Give a bounding box for every gametocyte.
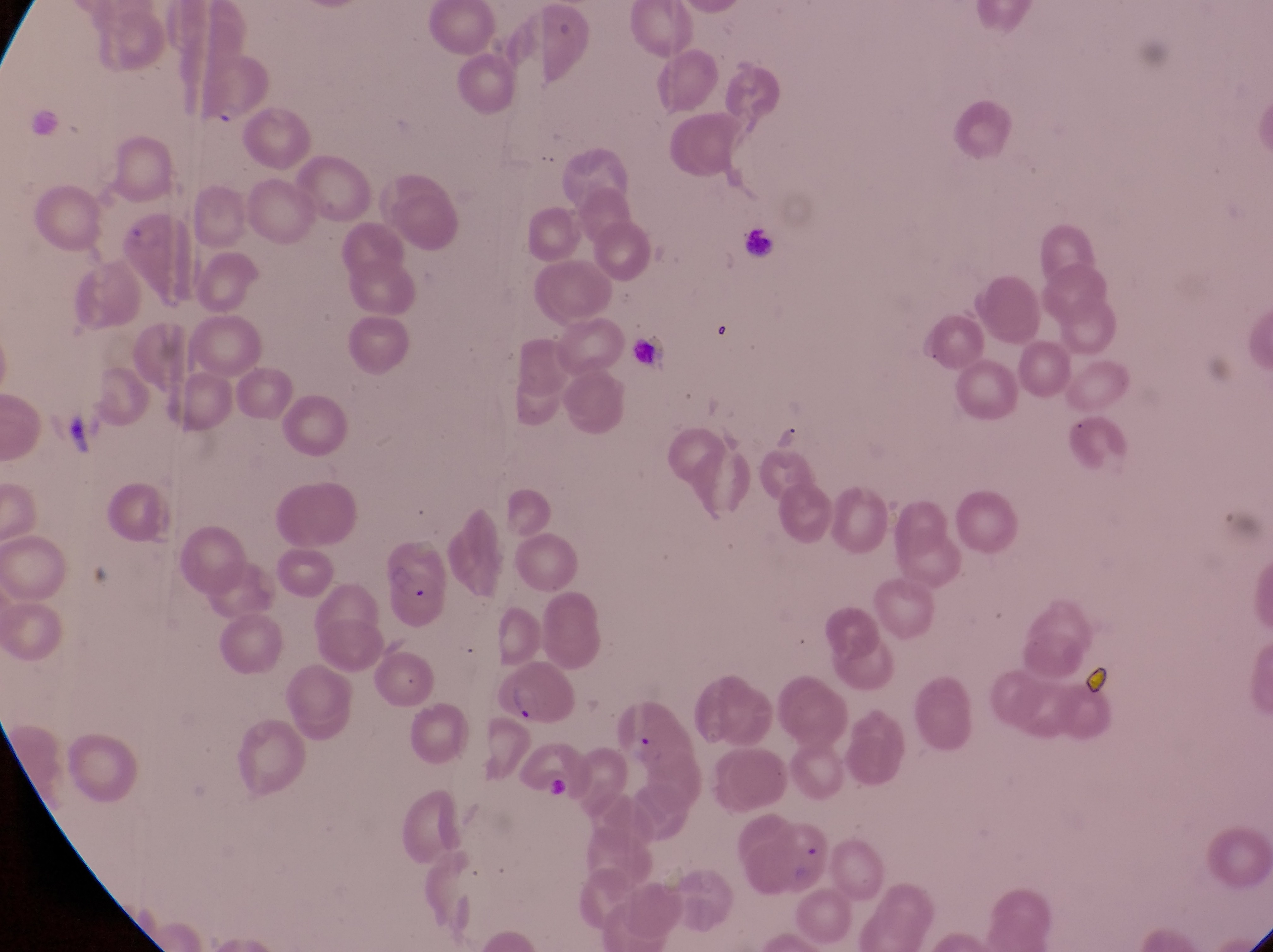

Approximate bounding boxes as {left, top, right, bottom} in pixels.
Gametocytes: {52, 410, 102, 460}.

Parasitised red blood cell locations: {492, 659, 582, 729}. Collected in Uganda. Image is 1273×952 pixels. Thin blood smear. Single field of view. Magnification of 1000x. Captured by a smartphone held over the eyepiece of an Olympus CX-23 microscope.